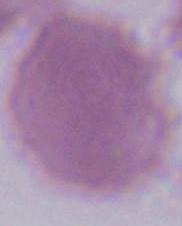

A red blood cell is seen. Micrograph. 1000x magnification.